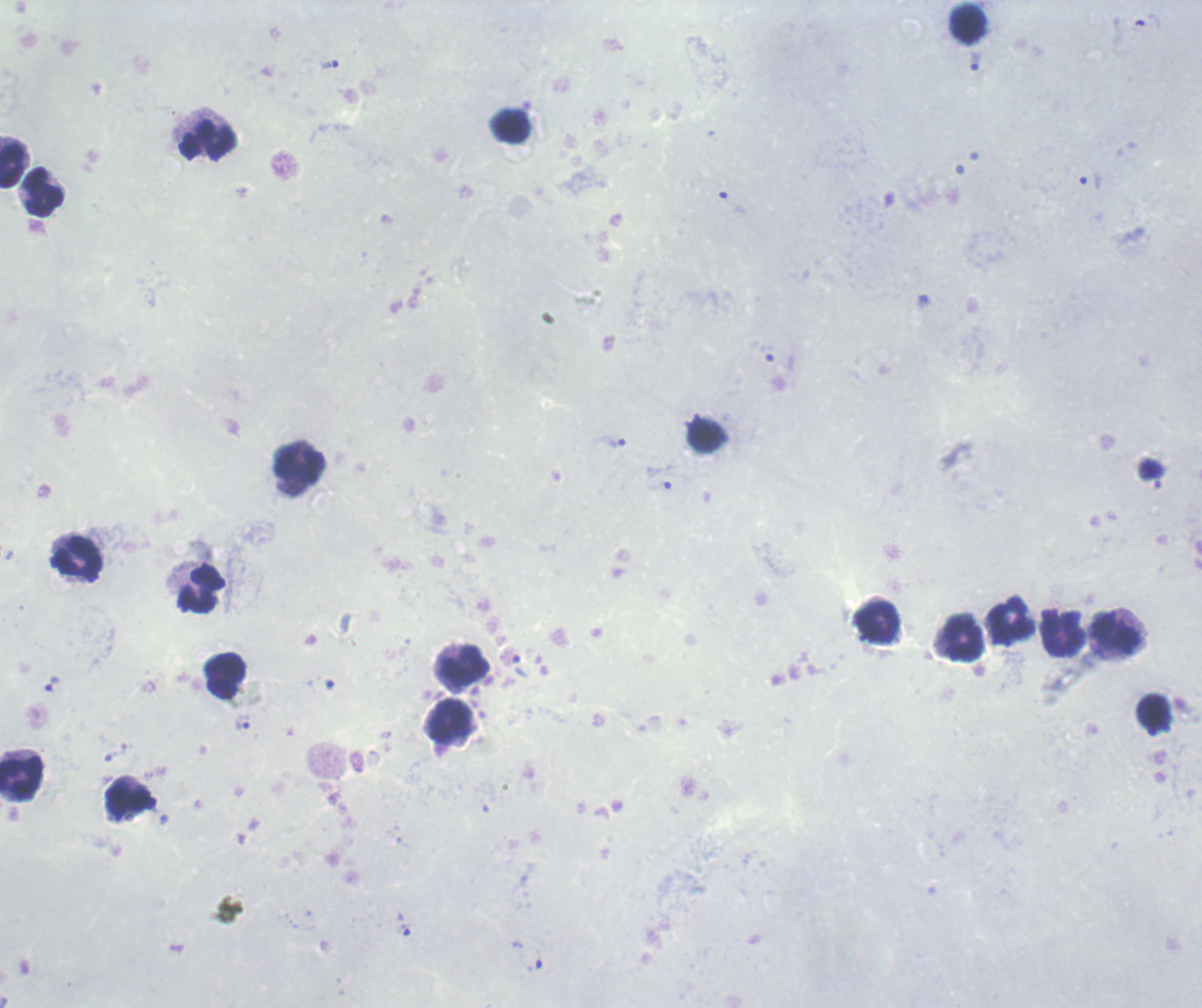

Approximate centers as {x, y} in pixels.
Summary:
  - Trophozoite locations: {974, 61}, {330, 65}, {1091, 181}, {611, 441}, {521, 666}, {52, 684}, {242, 722}, {404, 929}, {534, 960}
  - Leukocyte locations: {968, 23}, {511, 127}, {208, 141}, {14, 161}, {44, 193}, {706, 436}, {300, 463}, {77, 559}, {200, 589}, {1010, 620}, {877, 623}, {1063, 633}, {1117, 633}, {964, 637}, {462, 667}, {225, 677}, {1154, 713}, {449, 720}, {21, 777}, {131, 800}
  - Preparation: thick smear of blood
  - Result: Plasmodium parasites detected
  - Background quality: poor
  - Magnification: 100x
  - Stain: Romanowsky
  - Context: previously used in a real diagnosis
  - Image size: 1202×1008 pixels
  - Field of view: single